Assess for malaria.
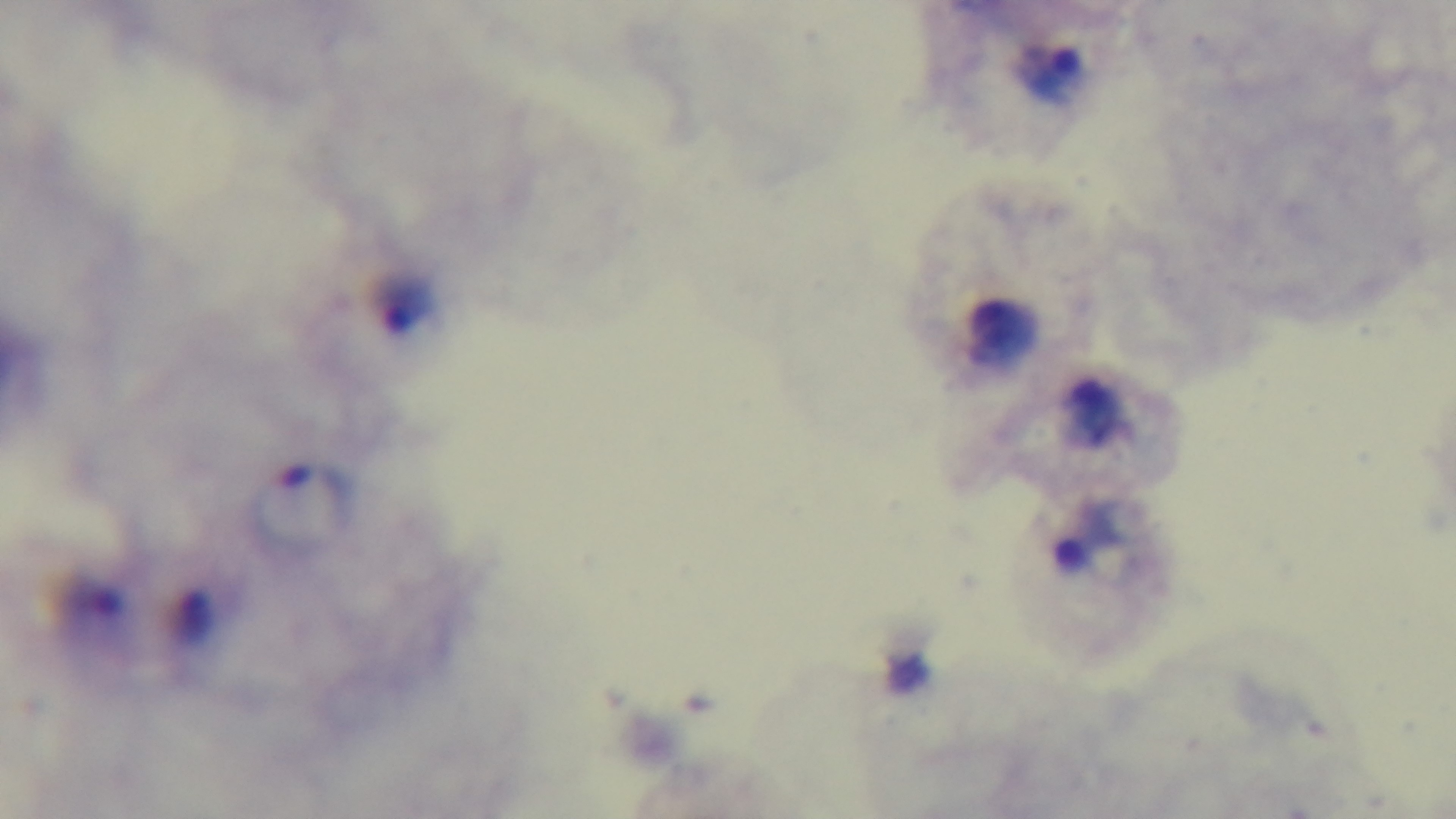

Infected.

field of view = one from the slide
capture = mounted 4K digital camera
preparation = thick smear
stain = Giemsa
modality = light microscopy
objective = 100x oil immersion